Locate every blood parasite and identify its species.
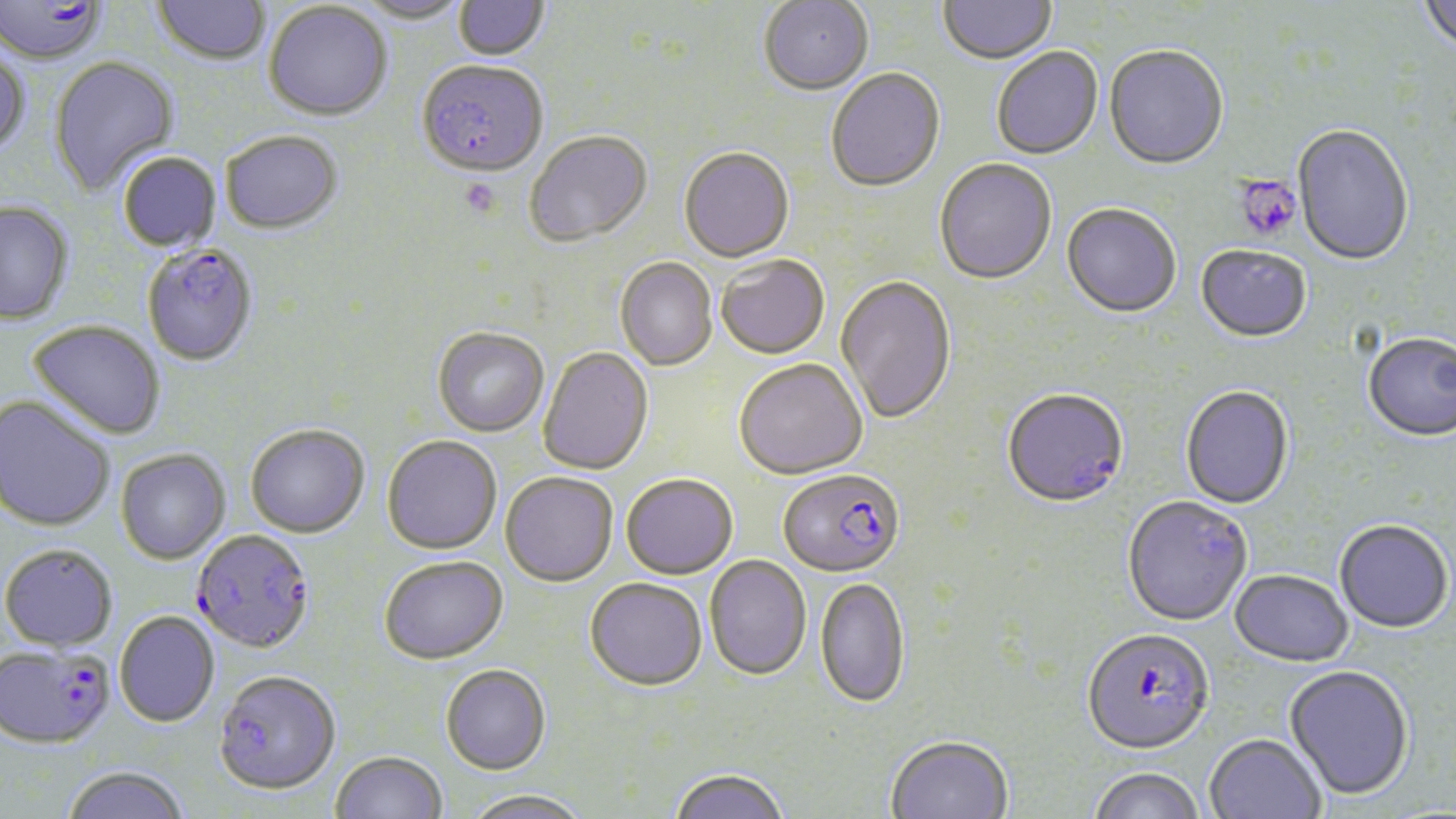
Approximate bounding boxes as (x1, y1, x2, y2) in pixels.
Plasmodium falciparum-infected red blood cells: (0, 0, 105, 65), (417, 62, 548, 179), (142, 245, 258, 366), (1002, 390, 1129, 511), (778, 470, 905, 580), (1122, 497, 1253, 628), (191, 529, 316, 656), (1082, 631, 1215, 758), (0, 645, 115, 751), (213, 672, 341, 798).
No Plasmodium ovale, Plasmodium malariae, Plasmodium vivax, Babesia divergens, or Trypanosoma brucei observed.

Uninfected red blood cell locations: (153, 0, 270, 66), (354, 0, 471, 26), (453, 0, 550, 62), (939, 0, 1056, 67), (1418, 0, 1456, 56), (758, 1, 873, 98), (263, 2, 392, 122), (1104, 47, 1229, 172), (992, 48, 1104, 161), (0, 49, 30, 157), (48, 56, 180, 196), (826, 70, 946, 194), (1292, 125, 1414, 268), (221, 132, 343, 236), (525, 132, 652, 247), (679, 149, 794, 264), (118, 153, 221, 253), (934, 160, 1057, 286), (0, 202, 75, 326), (1061, 205, 1181, 321), (1196, 246, 1311, 345), (716, 257, 830, 361), (615, 258, 718, 372), (835, 277, 956, 426), (28, 320, 166, 440), (432, 328, 549, 437), (1363, 335, 1456, 444), (537, 347, 654, 476), (734, 361, 867, 481), (1180, 387, 1294, 510), (0, 396, 115, 532), (245, 425, 369, 539), (381, 436, 502, 556), (116, 449, 231, 564), (500, 472, 618, 587), (621, 476, 738, 581), (1334, 521, 1453, 635), (1, 544, 118, 652), (704, 556, 811, 682), (378, 558, 509, 667), (1229, 572, 1353, 668), (815, 577, 910, 710), (585, 580, 707, 693), (114, 612, 220, 728), (440, 665, 551, 776), (1284, 667, 1414, 802), (885, 736, 1013, 819), (1204, 736, 1326, 819), (330, 752, 448, 819), (61, 767, 191, 819), (669, 769, 790, 819), (1087, 769, 1206, 819), (462, 790, 594, 819). Platelet locations: (459, 177, 502, 219), (1241, 178, 1302, 239). Slide-level diagnosis: Plasmodium falciparum. Thin blood smear. Optical microscopy. 1000x magnification. Single field of view. Image is 1456×819 pixels. May-Grünwald-Giemsa-stained preparation.